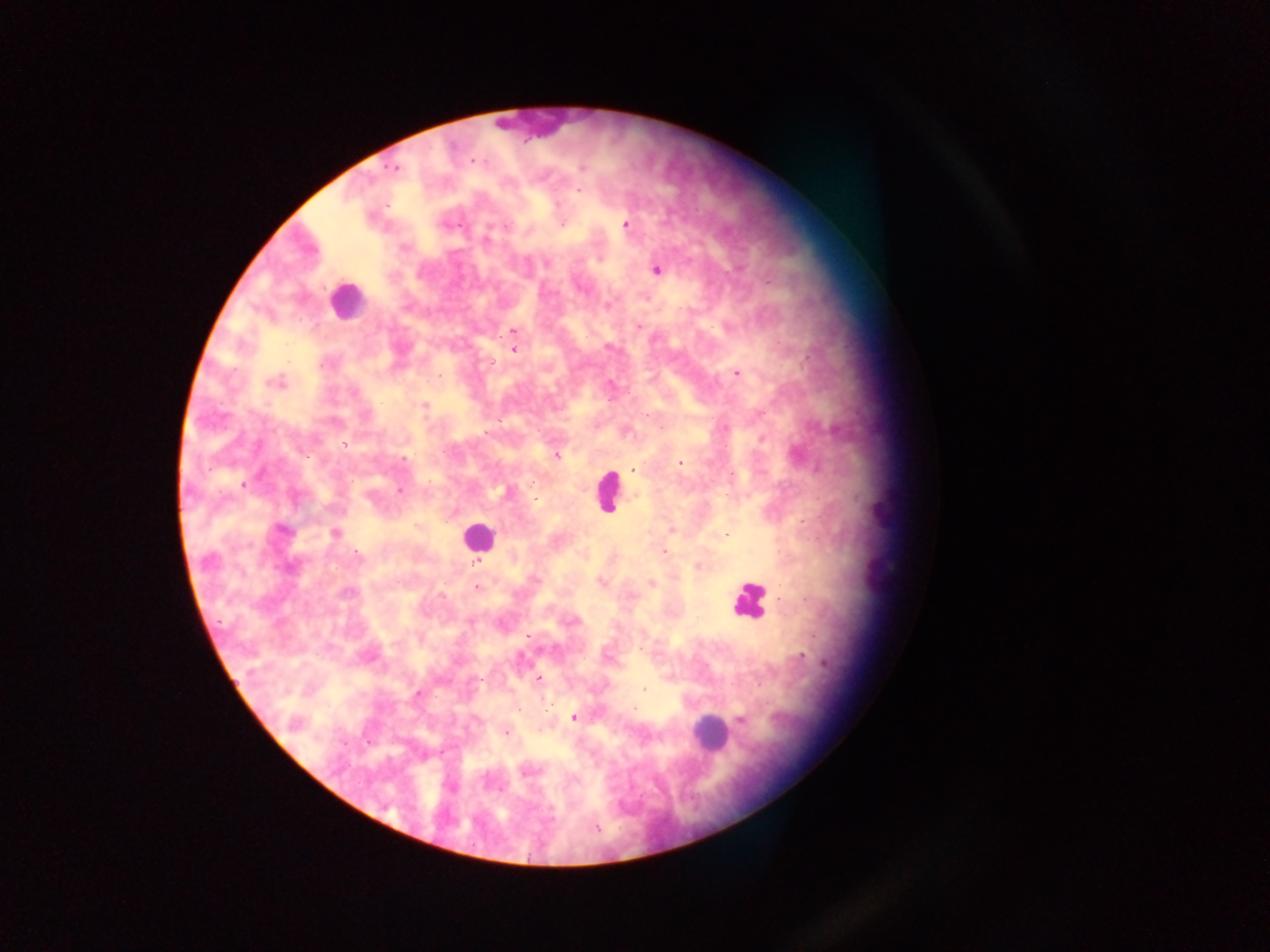

Approximate centers as x y in pixels.
Summary:
  - Malaria parasite locations: 475 161; 393 168; 582 168; 579 191; 626 224; 461 225; 561 225; 487 239; 404 247; 547 263; 656 271; 637 326; 513 332; 513 350; 736 373; 276 382; 424 405; 838 431; 345 444; 557 456; 403 458; 681 462; 633 469; 243 484; 400 490; 283 531; 335 532; 726 534; 665 553; 358 557; 208 560; 478 562; 698 566; 537 580; 601 583; 652 583; 477 587; 347 593; 442 595; 529 636; 641 649; 801 656; 539 678; 644 689; 418 693; 636 708; 574 717; 742 721; 295 723; 506 732; 526 771; 597 827
  - Leukocyte locations: 543 124; 347 301; 607 491; 477 535; 749 599; 709 732
  - Field of view: single
  - Preparation: thick blood smear
  - Country: Ghana
  - Capture: mobile-phone photograph through a microscope
  - Image size: 1270×952 pixels